State the preparation type.
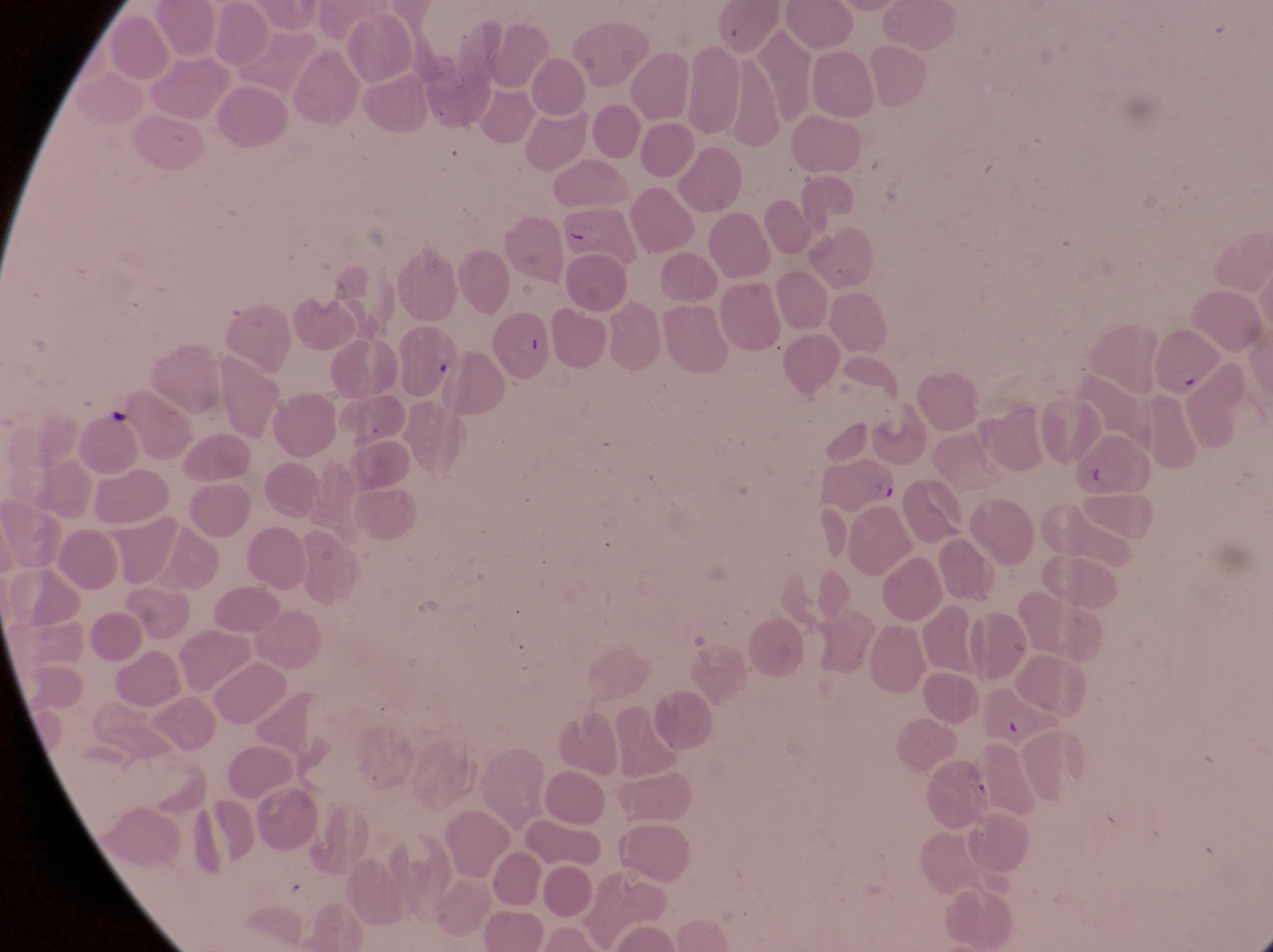

Thin blood film.

Approximate bounding boxes as (left, top, right, bottom) in pixels.
Summary:
  - Artifact (platelet-like body, stain precipitate, or debris) locations: (1171, 369, 1206, 396), (1085, 460, 1108, 495)
  - Parasitised red blood cell locations: (492, 312, 552, 386), (809, 455, 904, 517)
  - Country: Uganda
  - Magnification: 1000x
  - Image size: 1273×952 pixels
  - Capture: smartphone photograph through the eyepiece of an Olympus CX-23 microscope
  - Field of view: single